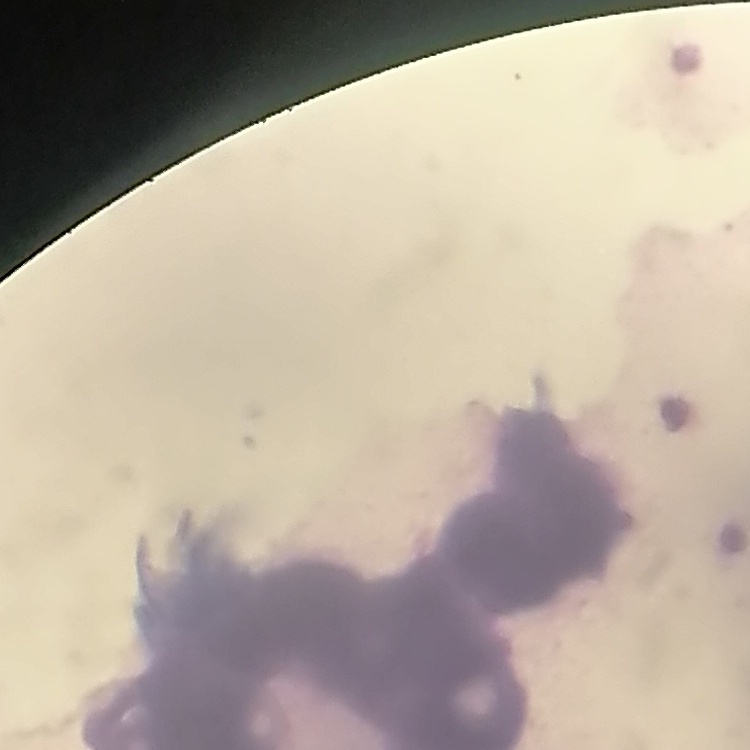

{
  "red_blood_cell_morphology": "rouleaux formation",
  "image_type": "one tile cut from a larger photomicrograph",
  "preparation": "thin blood film",
  "stain": "Field's or Giemsa"
}